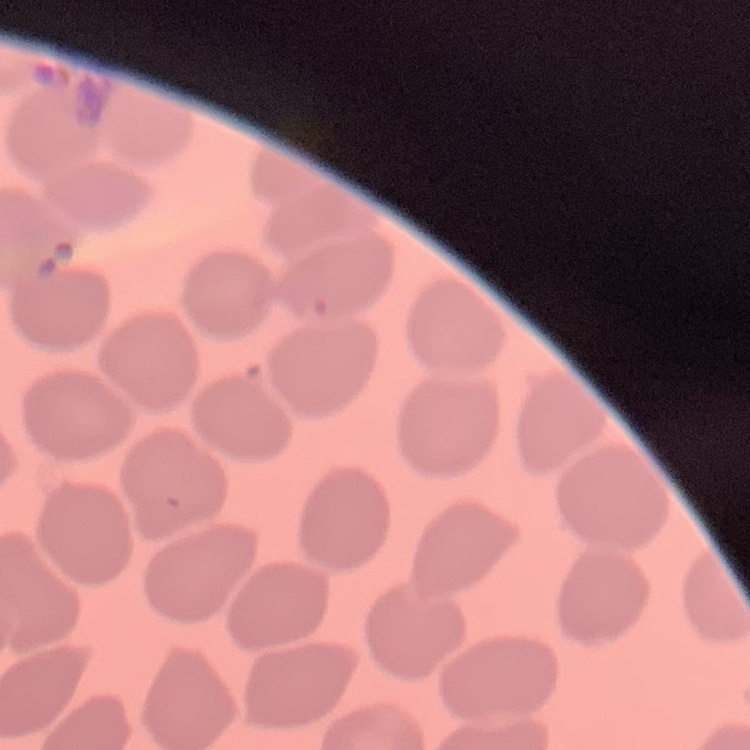

Summary:
  - Erythrocyte morphology: no rouleaux formation
  - Stain: Field's or Giemsa
  - Image type: square crop of a larger photomicrograph
  - Preparation: thin blood smear